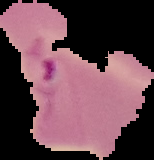
Summary:
  - Preparation: thin blood film
  - Image size: 154×160 pixels
  - Image type: segmented cell region on a black background
  - Result: Plasmodium parasites detected